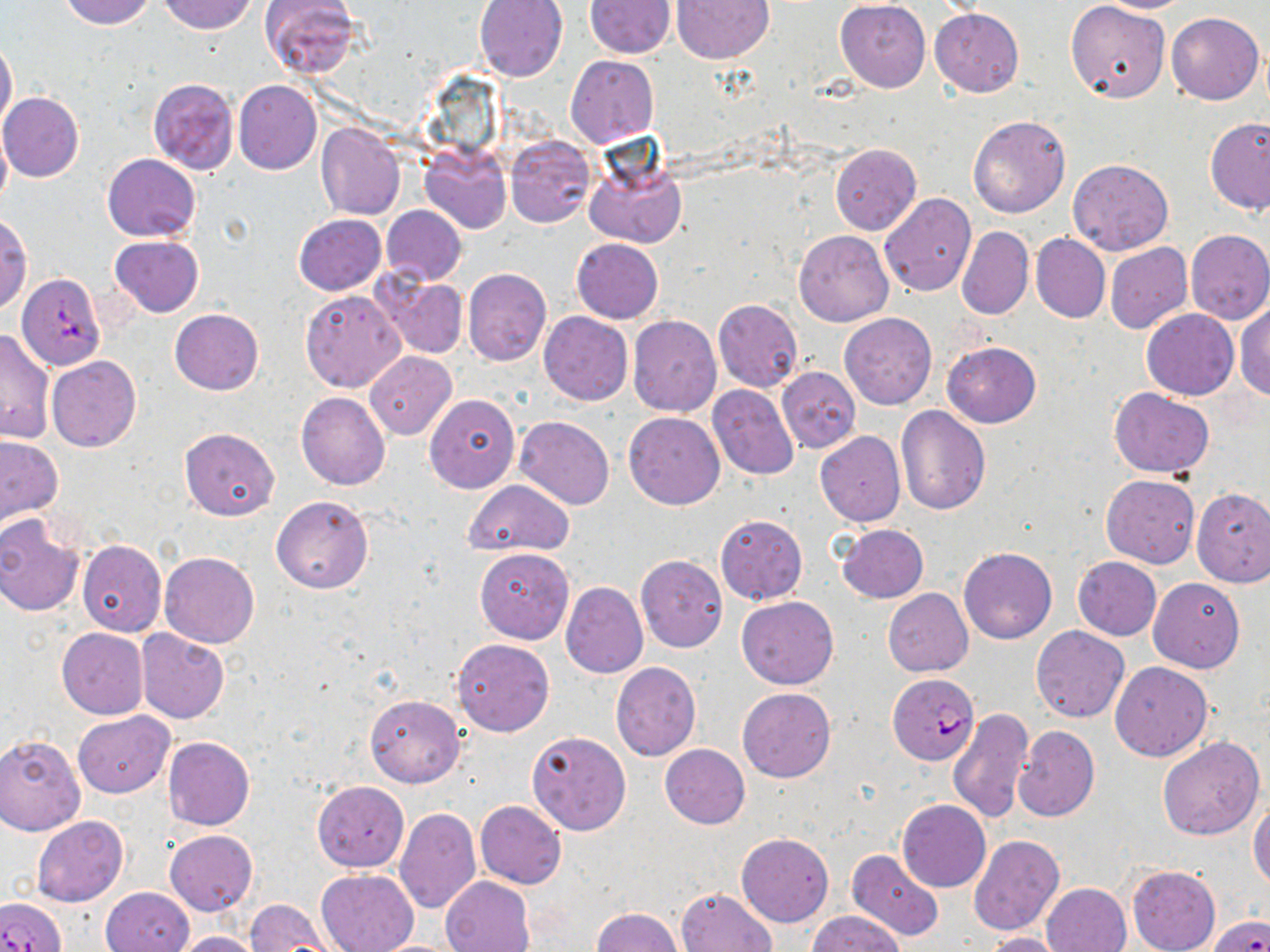

Summary:
  - Coordinate format: approximate bounding boxes as (x1,y1)-(x2,y2) corner pairs in pixels
  - Plasmodium falciparum-infected red blood cell locations: (17,273)-(106,370), (888,674)-(979,765), (0,896)-(66,952), (1208,915)-(1269,952)
  - Uninfected red blood cell locations: (59,0)-(153,29), (157,0)-(258,34), (259,0)-(360,78), (473,0)-(568,82), (672,0)-(773,63), (835,0)-(931,92), (1099,0)-(1194,12), (584,1)-(674,57), (1066,2)-(1171,104), (930,8)-(1024,96), (1166,11)-(1264,105), (0,37)-(17,132), (565,54)-(659,147), (148,78)-(239,175), (234,80)-(321,175), (1,92)-(84,182), (968,115)-(1070,218), (1206,116)-(1270,215), (316,123)-(404,220), (0,127)-(11,212), (505,135)-(595,227), (831,144)-(921,234), (420,146)-(511,234), (582,150)-(687,249), (102,153)-(201,242), (1068,159)-(1173,256), (879,193)-(976,297), (381,205)-(466,285), (292,213)-(386,296), (1,216)-(31,313), (957,227)-(1033,320), (1185,228)-(1269,324), (795,231)-(894,327), (1031,233)-(1110,323), (108,236)-(203,317), (571,238)-(663,323), (1105,243)-(1191,335), (462,268)-(553,366), (374,273)-(468,358), (300,288)-(406,392), (713,300)-(803,392), (1234,301)-(1270,403), (1141,308)-(1239,399), (171,309)-(263,395), (538,312)-(632,405), (839,313)-(936,409), (628,316)-(721,416), (0,327)-(55,446), (943,342)-(1041,427), (364,351)-(456,439), (47,356)-(141,452), (776,367)-(860,454), (707,385)-(800,481), (1109,388)-(1215,478), (296,392)-(390,490), (424,393)-(520,492), (895,406)-(991,516), (624,411)-(724,509), (515,416)-(615,510), (179,427)-(280,520), (815,431)-(905,526), (0,436)-(63,526), (1101,474)-(1199,567), (463,479)-(574,558), (1108,485)-(1270,582), (1192,488)-(1270,588), (272,494)-(373,595), (715,513)-(808,605), (0,515)-(85,617), (837,524)-(929,603), (77,540)-(167,637), (959,547)-(1057,643), (475,548)-(574,644), (159,551)-(261,648), (635,554)-(727,652), (1072,556)-(1161,640), (1148,576)-(1245,673), (561,583)-(648,678), (883,588)-(973,676), (737,595)-(839,689), (1031,626)-(1128,723), (56,628)-(149,718), (137,630)-(229,723), (452,638)-(554,736), (1110,661)-(1213,762), (610,662)-(700,761), (738,688)-(835,782), (365,695)-(465,787), (948,708)-(1034,823), (72,711)-(173,798), (1012,726)-(1100,822), (526,731)-(631,835), (0,735)-(86,835), (162,736)-(255,830), (1158,737)-(1264,840), (659,744)-(750,829), (313,781)-(409,872), (475,800)-(566,889), (897,800)-(991,892), (1249,800)-(1270,888), (394,809)-(481,914), (32,816)-(128,907), (165,829)-(256,916), (736,833)-(833,926), (969,834)-(1064,935), (848,849)-(945,941), (1127,864)-(1221,952), (315,870)-(419,952), (440,875)-(534,952), (1043,882)-(1131,952), (102,887)-(194,952), (676,887)-(776,951), (245,898)-(334,949), (593,907)-(683,952), (807,910)-(905,951), (171,931)-(264,952), (982,932)-(1070,952)
  - Slide-level diagnosis: Plasmodium falciparum
  - Magnification: 1000x
  - Stain: May-Grünwald-Giemsa
  - Image size: 1270×952 pixels
  - Field of view: single
  - Preparation: thin blood smear
  - Modality: optical microscopy